Outline each blood parasite and name the species.
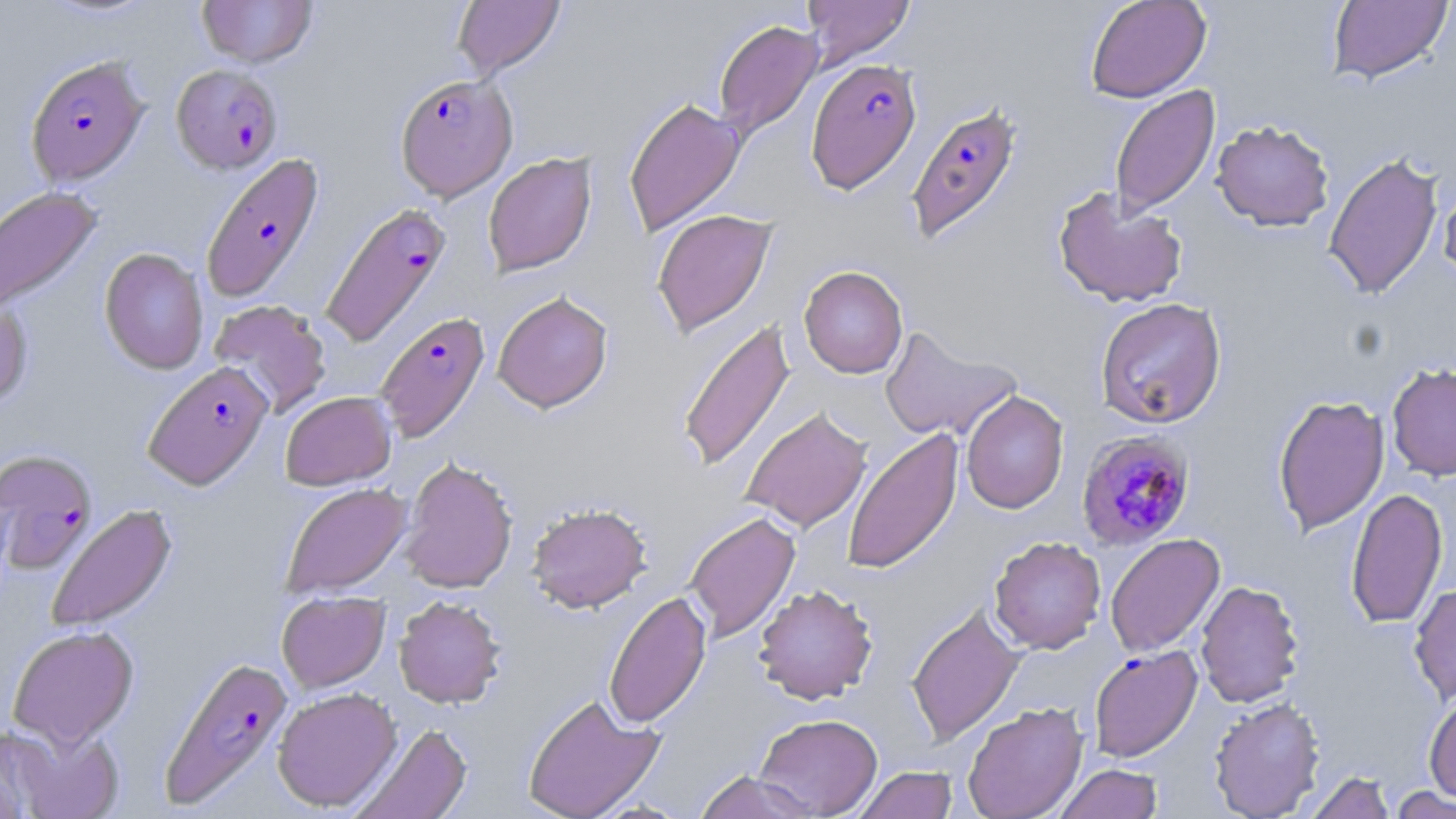

Approximate bounding boxes as (x1, y1, x2, y2) in pixels.
Plasmodium falciparum-infected red blood cells (subset): (25, 55, 149, 187), (805, 58, 922, 194), (171, 63, 283, 174), (394, 73, 517, 201), (905, 101, 1023, 244), (201, 152, 326, 303), (320, 202, 452, 348), (375, 311, 491, 443), (143, 360, 273, 489), (1077, 429, 1196, 551), (1088, 645, 1202, 763), (158, 654, 293, 810).
No Plasmodium ovale, Plasmodium malariae, Plasmodium vivax, Babesia divergens, or Trypanosoma brucei observed.

Uninfected red blood cell locations (subset): (196, 0, 317, 68), (452, 0, 565, 79), (801, 0, 915, 68), (1085, 0, 1211, 103), (1326, 1, 1453, 85), (713, 19, 824, 140), (1110, 85, 1220, 220), (623, 96, 745, 238), (1211, 119, 1335, 231), (1323, 151, 1444, 300), (483, 152, 597, 277), (1438, 176, 1456, 285), (0, 185, 103, 315), (1051, 187, 1188, 309), (651, 208, 778, 338), (99, 248, 208, 374), (799, 265, 908, 379), (493, 291, 613, 412), (0, 297, 33, 410), (1095, 297, 1226, 428), (208, 299, 333, 419), (677, 318, 796, 473), (880, 325, 1022, 443), (1386, 362, 1456, 481), (961, 390, 1068, 515), (280, 391, 397, 491), (1272, 394, 1389, 537), (741, 407, 872, 533), (842, 427, 964, 575), (399, 456, 518, 594), (280, 482, 412, 599), (1345, 486, 1448, 629), (526, 503, 652, 613), (45, 504, 177, 632), (684, 511, 801, 643), (1105, 533, 1225, 657), (989, 536, 1106, 654), (1195, 579, 1306, 708), (1409, 583, 1456, 705), (753, 584, 878, 704), (276, 591, 390, 692), (604, 591, 711, 729), (394, 595, 506, 708), (906, 603, 1025, 745), (7, 624, 139, 748), (272, 686, 402, 812), (1423, 691, 1456, 804), (522, 693, 665, 819), (1208, 697, 1325, 818), (962, 701, 1088, 819), (754, 713, 883, 818), (4, 722, 126, 819), (350, 722, 472, 819), (0, 726, 55, 818), (1054, 763, 1163, 819), (854, 766, 958, 819), (694, 769, 819, 819), (1305, 771, 1397, 818), (1388, 785, 1455, 818). Slide-level diagnosis: Plasmodium falciparum. 1000x magnification. May-Grünwald-Giemsa-stained preparation. Image is 1456×819 pixels. One field of a larger specimen. Thin blood smear. Optical microscopy.